Assess this cell for malaria.
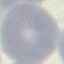

Uninfected.

Giemsa stain. Thin smear of blood. Cell patch, automatically extracted from a larger field of view and resized to 64 × 64 pixels. Acquired by smartphone through the microscope eyepiece.